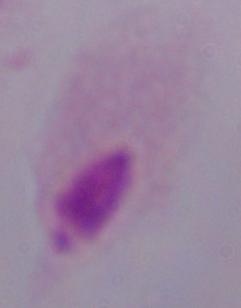 A trichomonad is shown. Micrograph. Captured at 1000x magnification.